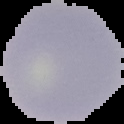

From a thin blood film. Result: no malaria parasites seen. Segmented cell region on a black background. Image is 124×124 pixels.